Report the malaria status of this cell.
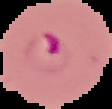
Parasitized.

Summary:
  - Image size: 112×109 pixels
  - Preparation: thin blood film
  - Image type: segmented cell region on a black background